Evaluate for Plasmodium parasites.
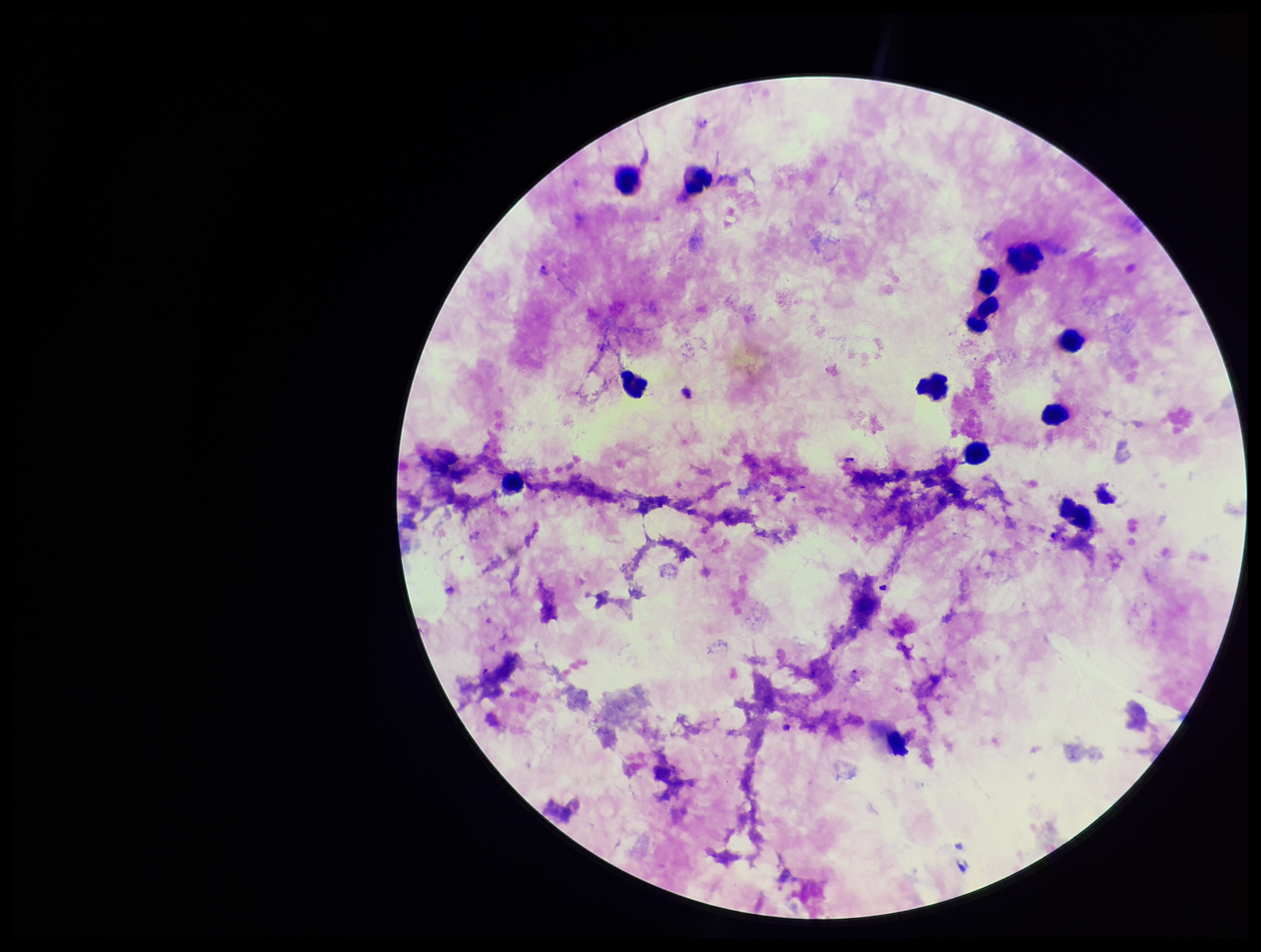

Detected.

Photographed through the microscope eyepiece with a smartphone camera. Stained with Giemsa. Parasite count: 2. Species reported for this patient: Plasmodium falciparum. Patient malaria status: positive. Leukocyte count: 14. One field from this slide. Preparation: thick blood smear. Image is 1261×952 pixels.